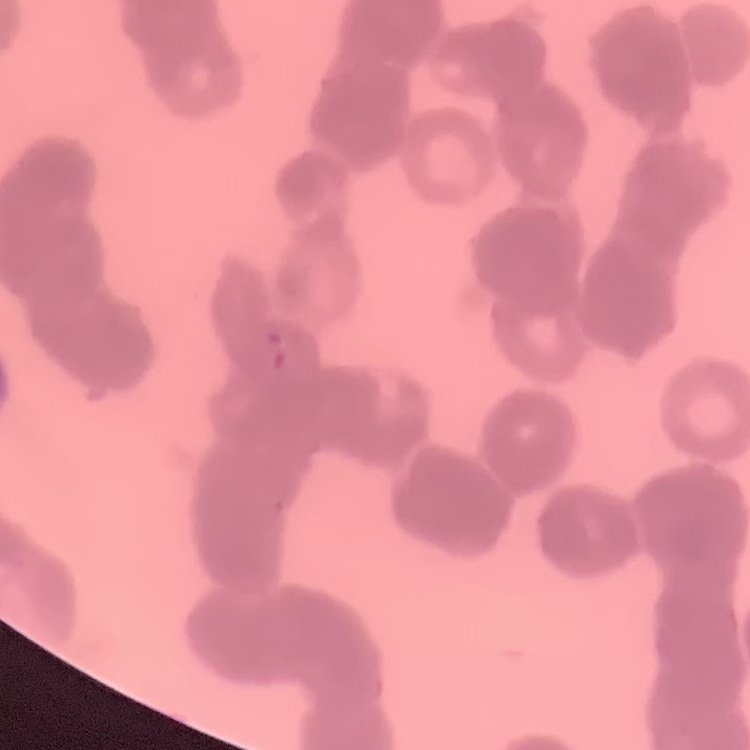

The red blood cells exhibit rouleaux formation. Square crop of a larger photomicrograph. Thin blood smear. Stained with either Field's or Giemsa.